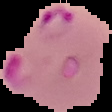
Image is 112×112 pixels. From a thin blood film. Segmented cell region on a black background. Result: Plasmodium parasites identified.